Outline each blood parasite and name the species.
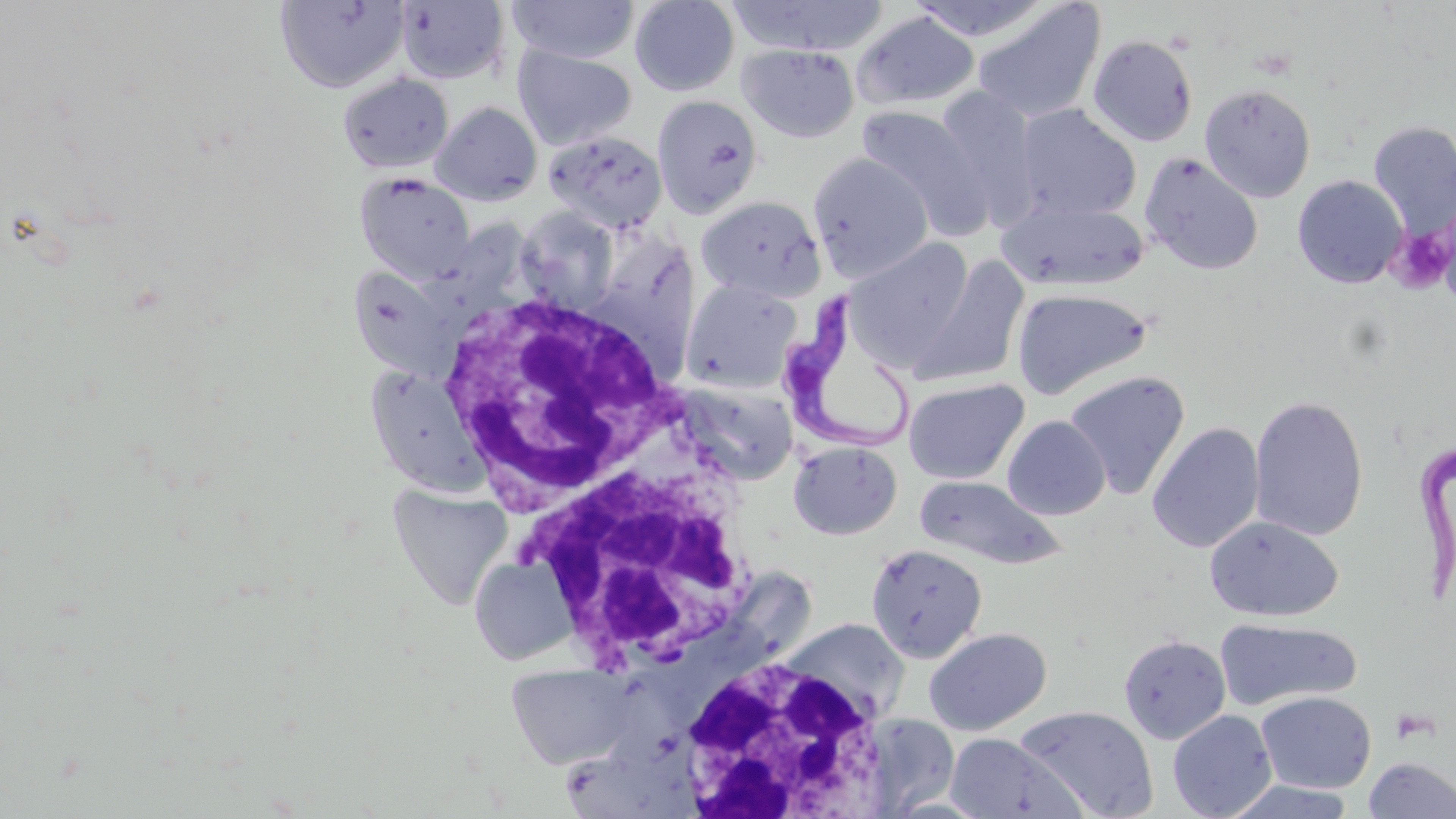

Approximate bounding boxes as (x1, y1, x2, y2) in pixels.
Trypanosoma brucei: (777, 295, 919, 456), (1415, 431, 1456, 605).
No Plasmodium falciparum, Plasmodium ovale, Plasmodium malariae, Plasmodium vivax, or Babesia divergens observed.

Summary:
  - Platelet locations: (1390, 225, 1454, 294)
  - White blood cell locations: (434, 291, 685, 516), (520, 426, 761, 674), (671, 652, 890, 815)
  - Uninfected red blood cell locations: (274, 0, 410, 94), (629, 0, 741, 96), (727, 0, 889, 57), (907, 0, 1057, 43), (394, 1, 511, 86), (506, 1, 641, 64), (972, 2, 1105, 125), (852, 11, 979, 110), (1088, 35, 1198, 146), (511, 44, 637, 151), (737, 44, 859, 143), (338, 71, 454, 175), (1199, 83, 1316, 202), (932, 86, 1043, 226), (651, 95, 763, 218), (430, 101, 543, 206), (856, 105, 992, 238), (1013, 105, 1141, 222), (1369, 121, 1456, 238), (543, 130, 668, 234), (809, 152, 933, 282), (1140, 153, 1264, 276), (354, 172, 476, 284), (1292, 174, 1408, 289), (694, 195, 826, 303), (997, 198, 1148, 292), (515, 206, 621, 312), (435, 219, 536, 313), (593, 231, 699, 355), (846, 239, 976, 368), (908, 256, 1029, 388), (347, 264, 465, 382), (682, 279, 803, 394), (1011, 287, 1153, 399), (1063, 370, 1190, 501), (675, 378, 800, 486), (903, 378, 1029, 485), (1249, 394, 1369, 541), (1002, 415, 1110, 520), (1147, 421, 1264, 553), (788, 441, 903, 540), (914, 475, 1065, 569), (386, 481, 511, 611), (1205, 517, 1342, 622), (865, 543, 987, 663), (469, 555, 576, 666), (1215, 616, 1361, 712), (780, 617, 909, 723), (924, 627, 1052, 735), (1118, 634, 1231, 744), (504, 661, 638, 770), (1255, 691, 1376, 793), (1015, 705, 1159, 819), (1167, 710, 1277, 819), (859, 715, 961, 815), (943, 733, 1087, 819), (1362, 757, 1456, 818), (1221, 780, 1359, 819)
  - Slide-level diagnosis: Trypanosoma brucei
  - Modality: optical microscopy
  - Stain: May-Grünwald-Giemsa
  - Preparation: thin blood film
  - Image size: 1456×819 pixels
  - Field of view: single
  - Magnification: 1000x